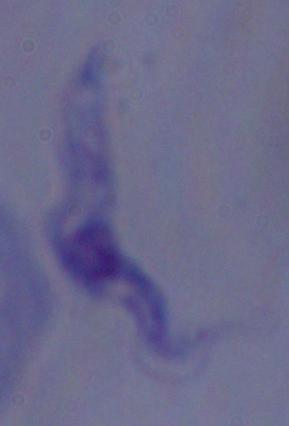

modality = micrograph
magnification = 1000x
identification = trypanosome